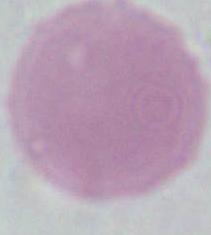
Micrograph. 1000x magnification. An erythrocyte is seen.